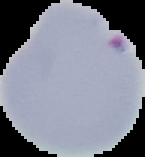

result = Plasmodium parasites identified
image size = 145×157 pixels
image type = segmented cell region on a black background
preparation = thin blood smear